Report the malaria status of this cell.
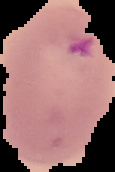
It is parasitized.

{
  "image_type": "segmented cell region on a black background",
  "image_size": "115×172 pixels",
  "preparation": "thin blood smear"
}